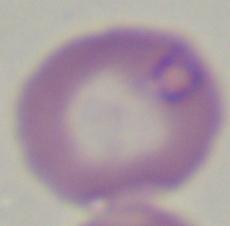

Photomicrograph. Captured at 1000x magnification. A Babesia parasite is shown.